Assess the morphology of the erythrocytes.
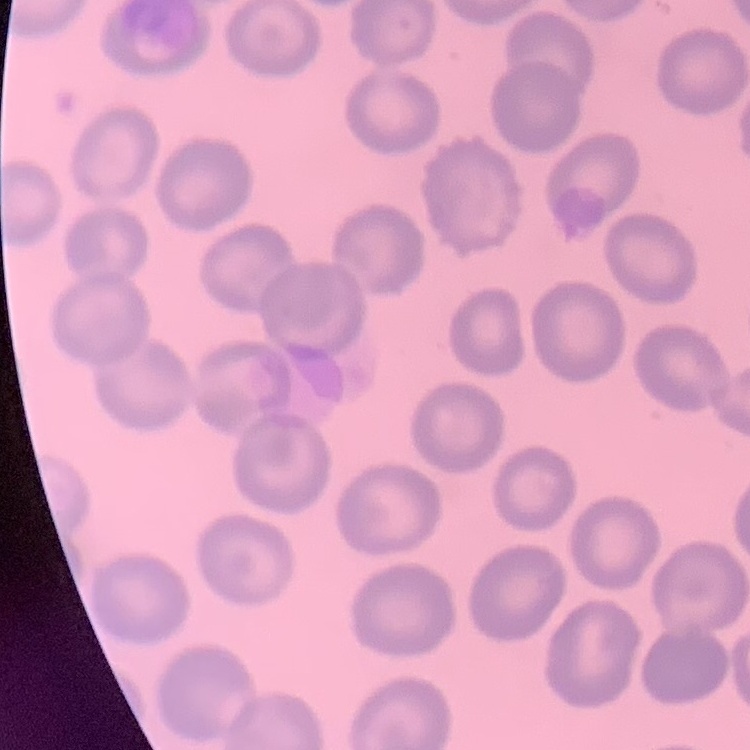
No rouleaux formation.

preparation = thin peripheral smear
image type = square crop of a larger photomicrograph
stain = Field's or Giemsa